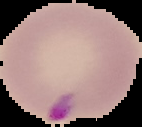 Image is 142×127 pixels. From a thin blood film. Malaria status: parasitized. Segmented cell region on a black background.